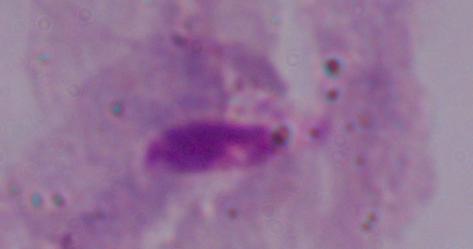
Photomicrograph. A trichomonad is shown. Captured at 1000x magnification.